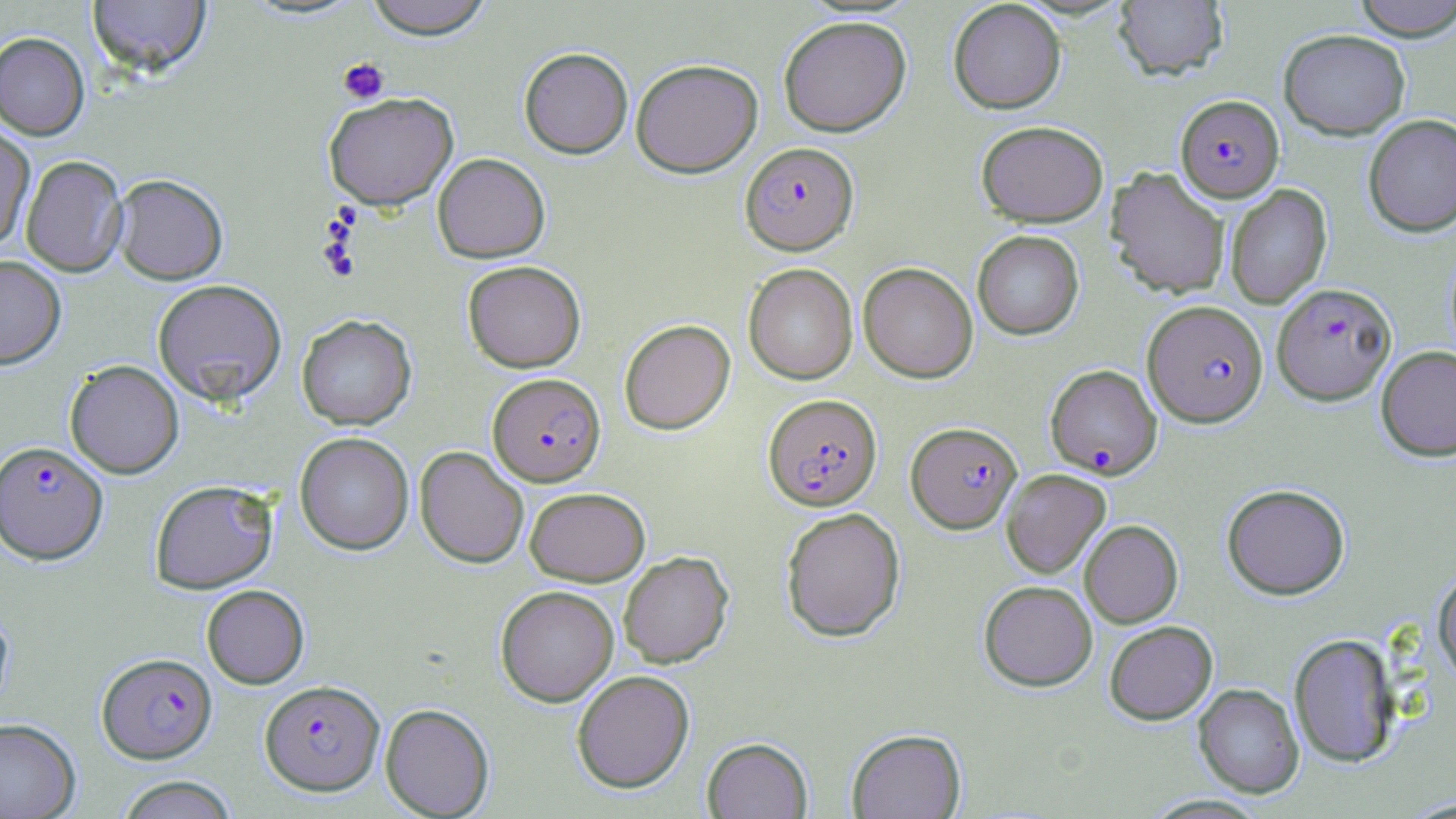

slide_level_diagnosis: Plasmodium falciparum
uninfected_red_blood_cell_locations: 'approximate bounding boxes as (x1,y1)-(x2,y2) corner pairs in pixels: (362,0)-(494,39), (1351,0)-(1456,40), (86,1)-(211,79), (948,1)-(1066,113), (1113,1)-(1228,81), (778,15)-(911,137), (1278,29)-(1411,139), (0,32)-(90,140), (519,47)-(633,158), (631,58)-(763,177), (323,92)-(458,210), (1363,114)-(1456,238), (976,120)-(1108,226), (0,124)-(35,249), (432,153)-(550,263), (20,154)-(128,277), (1106,167)-(1230,299), (112,173)-(228,285), (1225,184)-(1332,309), (972,230)-(1084,340), (0,255)-(66,369), (462,260)-(586,372), (858,262)-(978,383), (743,263)-(858,385), (153,279)-(287,406), (297,314)-(417,430), (619,318)-(735,434), (1376,345)-(1456,461), (64,360)-(184,478), (295,432)-(414,555), (415,446)-(529,568), (1001,469)-(1111,578), (150,479)-(278,593), (1222,483)-(1350,599), (524,487)-(650,585), (780,507)-(906,642), (1079,520)-(1183,627), (618,551)-(734,669), (1432,570)-(1456,685), (979,580)-(1097,691), (201,584)-(309,689), (495,585)-(619,706), (0,601)-(14,719), (1104,620)-(1218,724), (1288,633)-(1400,767), (571,670)-(695,793), (1193,683)-(1304,798), (380,703)-(494,818), (0,718)-(81,819), (846,728)-(966,819), (702,737)-(813,818), (114,775)-(239,819)'
platelet_locations: 'approximate bounding boxes as (x1,y1)-(x2,y2) corner pairs in pixels: (338,57)-(389,104)'
preparation: thin blood smear
stain: May-Grünwald-Giemsa
image_size: 1456×819 pixels
magnification: 1000x
field_of_view: single
plasmodium_falciparum_infected_red_blood_cell_locations: 'approximate bounding boxes as (x1,y1)-(x2,y2) corner pairs in pixels: (1175,95)-(1284,202), (740,141)-(858,254), (1271,282)-(1397,404), (1143,300)-(1268,427), (1045,364)-(1162,478), (488,373)-(606,486), (763,393)-(882,510), (906,421)-(1022,533), (0,440)-(108,564), (97,652)-(217,763), (259,679)-(385,795)'
modality: light microscopy